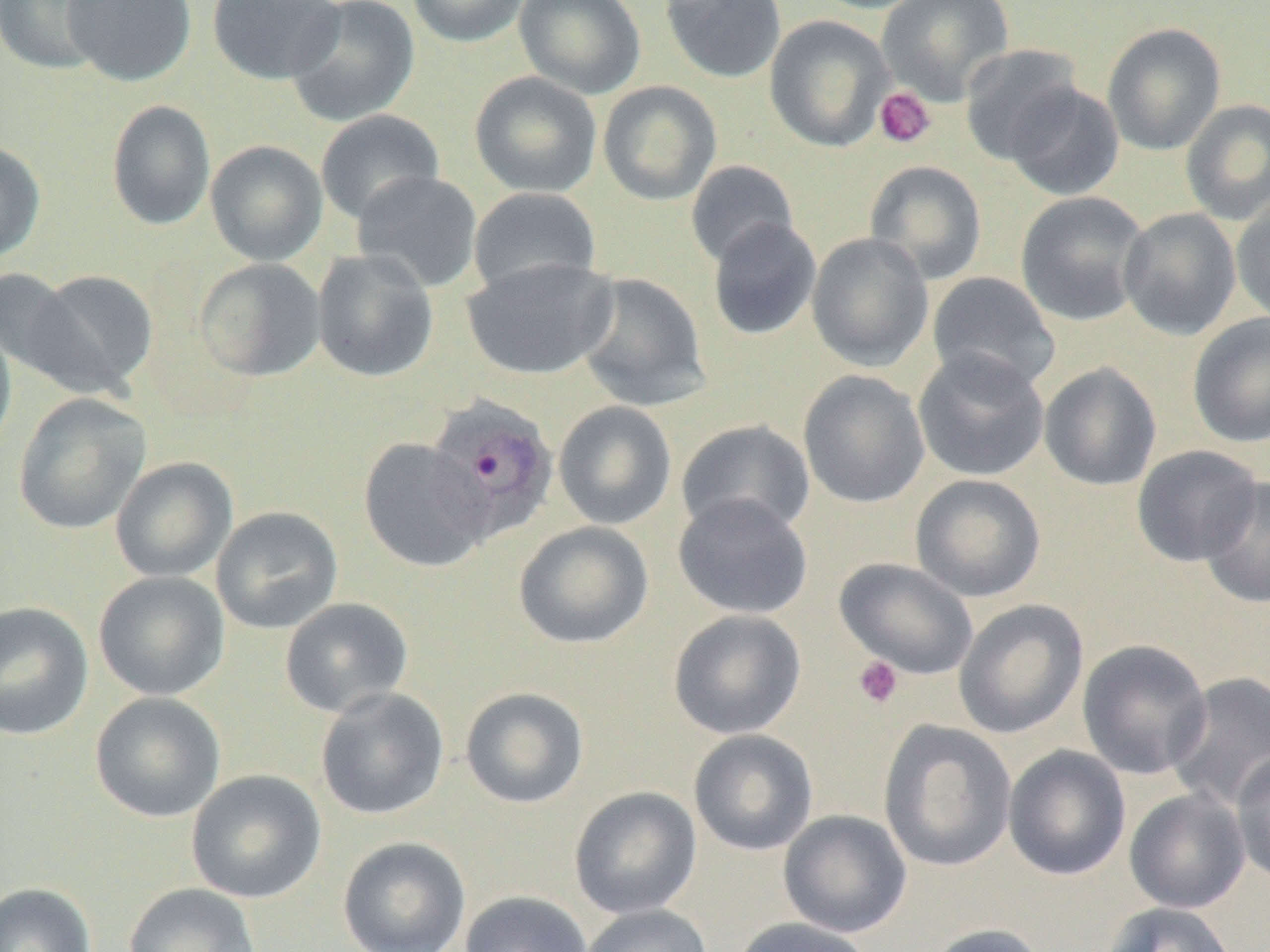
{
  "plasmodium_ovale_infected_red_blood_cell_locations": "approximate bounding boxes as (x1, y1, x2, y2) in pixels: (424, 395, 559, 541)",
  "slide_level_diagnosis": "Plasmodium ovale",
  "modality": "optical microscopy",
  "field_of_view": "one of a larger specimen",
  "magnification": "1000x",
  "uninfected_red_blood_cell_locations": "approximate bounding boxes as (x1, y1, x2, y2) in pixels: (0, 0, 112, 74), (61, 0, 196, 86), (207, 0, 345, 85), (284, 0, 420, 128), (406, 0, 531, 48), (514, 0, 646, 99), (659, 0, 787, 83), (808, 0, 933, 14), (876, 0, 1014, 104), (765, 15, 895, 151), (1102, 22, 1226, 156), (959, 43, 1085, 165), (469, 71, 603, 198), (598, 81, 722, 205), (1005, 82, 1125, 201), (1180, 98, 1270, 225), (106, 100, 216, 230), (315, 110, 445, 225), (0, 139, 46, 263), (205, 140, 328, 265), (685, 160, 799, 267), (864, 160, 987, 285), (352, 170, 483, 292), (468, 187, 602, 298), (1231, 190, 1270, 325), (1015, 191, 1151, 327), (1118, 207, 1241, 340), (706, 218, 822, 341), (806, 232, 934, 372), (312, 249, 439, 383), (461, 257, 618, 380), (194, 258, 327, 382), (0, 268, 82, 381), (25, 269, 158, 397), (926, 271, 1061, 395), (574, 273, 711, 412), (1188, 312, 1270, 449), (0, 316, 17, 460), (912, 348, 1050, 482), (1039, 361, 1162, 492), (798, 370, 930, 508), (13, 393, 151, 535), (553, 401, 677, 530), (676, 419, 816, 537), (358, 437, 491, 572), (1132, 445, 1263, 566), (110, 457, 238, 583), (910, 474, 1046, 602), (1199, 475, 1270, 609), (672, 494, 814, 620), (210, 506, 344, 634), (513, 521, 653, 649), (834, 558, 979, 679), (93, 571, 230, 701), (279, 597, 414, 718), (953, 599, 1088, 738), (0, 601, 94, 740), (668, 609, 806, 739), (1076, 638, 1213, 780), (1166, 673, 1270, 811), (315, 686, 449, 821), (459, 686, 589, 809), (89, 691, 226, 823), (878, 720, 1017, 872), (688, 729, 819, 856), (1003, 745, 1131, 881), (1230, 749, 1270, 887), (185, 769, 327, 904), (569, 786, 702, 919), (1124, 788, 1251, 914), (778, 809, 912, 938), (336, 836, 471, 951), (0, 882, 97, 952), (122, 883, 261, 952), (459, 890, 592, 952), (1101, 902, 1237, 952), (580, 904, 714, 952), (729, 917, 876, 952), (924, 922, 1051, 952)",
  "image_size": "1270×952 pixels",
  "preparation": "thin blood smear",
  "platelet_locations": "approximate bounding boxes as (x1, y1, x2, y2) in pixels: (874, 86, 937, 149), (853, 655, 904, 709)"
}